Report the malaria status of this cell.
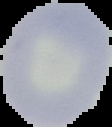
It is uninfected.

Summary:
  - Image size: 112×127 pixels
  - Preparation: thin blood film
  - Image type: segmented cell region with the area outside set to black